Outline platelets.
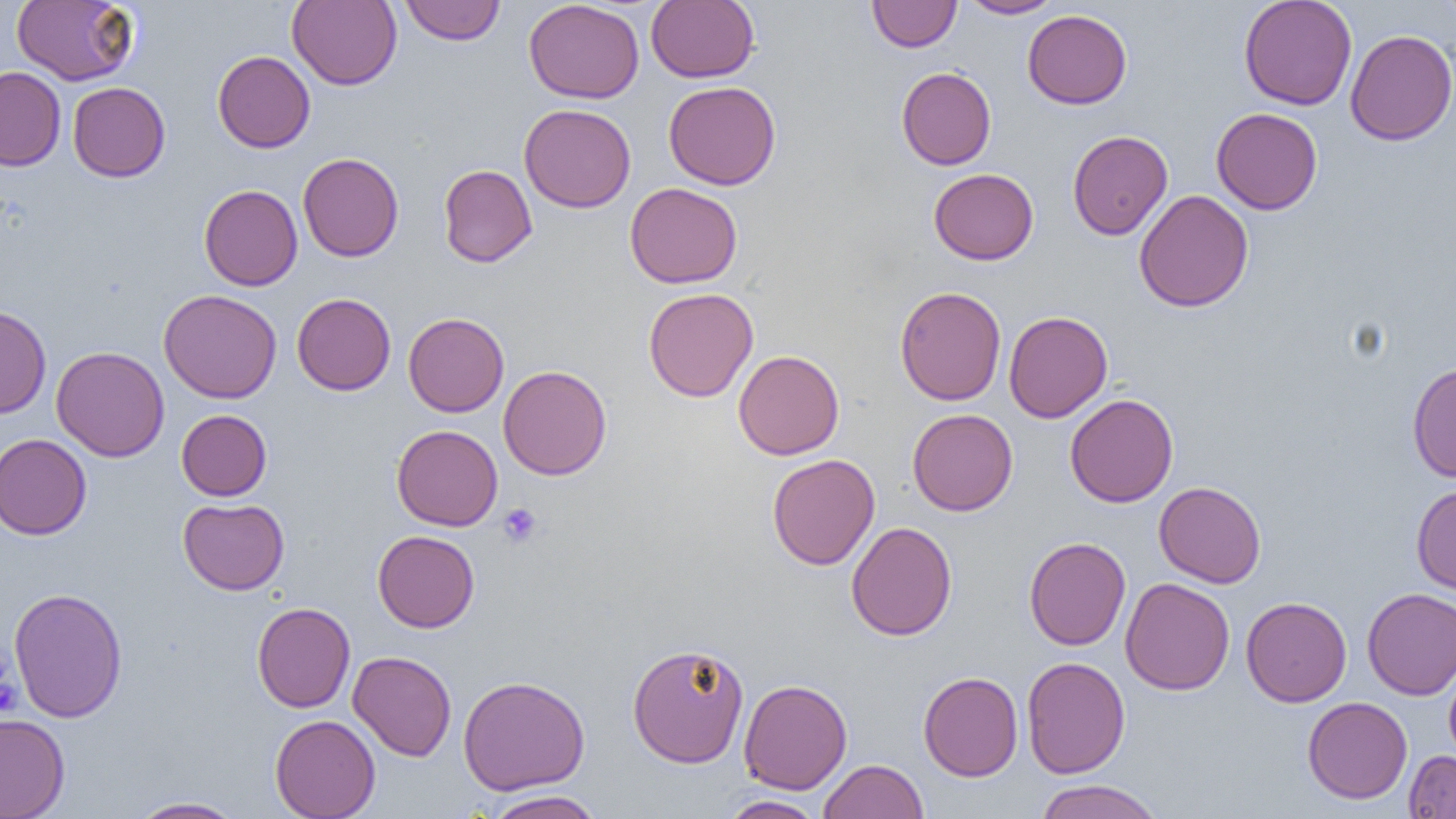

Approximate bounding boxes as named x1/y1/x2/y2 corners in pixels.
Platelets: (x1=498, y1=503, x2=543, y2=548).

Summary:
  - Uninfected red blood cell locations: (x1=11, y1=0, x2=139, y2=86), (x1=288, y1=0, x2=402, y2=90), (x1=400, y1=0, x2=505, y2=45), (x1=523, y1=0, x2=644, y2=103), (x1=867, y1=0, x2=961, y2=52), (x1=959, y1=0, x2=1063, y2=18), (x1=1239, y1=0, x2=1358, y2=110), (x1=1435, y1=0, x2=1456, y2=26), (x1=646, y1=1, x2=760, y2=83), (x1=1022, y1=9, x2=1132, y2=109), (x1=1345, y1=29, x2=1456, y2=146), (x1=212, y1=50, x2=315, y2=152), (x1=0, y1=67, x2=66, y2=171), (x1=896, y1=67, x2=996, y2=170), (x1=663, y1=81, x2=781, y2=190), (x1=68, y1=82, x2=170, y2=182), (x1=519, y1=104, x2=636, y2=213), (x1=1211, y1=108, x2=1323, y2=214), (x1=1067, y1=130, x2=1173, y2=240), (x1=298, y1=152, x2=404, y2=262), (x1=438, y1=164, x2=537, y2=267), (x1=929, y1=168, x2=1038, y2=265), (x1=624, y1=182, x2=743, y2=288), (x1=199, y1=184, x2=302, y2=291), (x1=1134, y1=189, x2=1254, y2=312), (x1=895, y1=286, x2=1006, y2=405), (x1=643, y1=287, x2=758, y2=402), (x1=158, y1=289, x2=282, y2=404), (x1=292, y1=293, x2=396, y2=395), (x1=0, y1=305, x2=52, y2=418), (x1=1004, y1=310, x2=1112, y2=423), (x1=403, y1=312, x2=509, y2=417), (x1=51, y1=345, x2=170, y2=462), (x1=733, y1=350, x2=845, y2=460), (x1=1407, y1=361, x2=1456, y2=483), (x1=498, y1=364, x2=612, y2=480), (x1=1065, y1=393, x2=1179, y2=507), (x1=177, y1=409, x2=272, y2=500), (x1=907, y1=409, x2=1018, y2=515), (x1=392, y1=424, x2=503, y2=531), (x1=0, y1=434, x2=92, y2=540), (x1=767, y1=453, x2=880, y2=570), (x1=1154, y1=481, x2=1266, y2=588), (x1=1411, y1=483, x2=1456, y2=596), (x1=177, y1=498, x2=289, y2=595), (x1=846, y1=521, x2=957, y2=641), (x1=372, y1=530, x2=480, y2=632), (x1=1024, y1=536, x2=1130, y2=650), (x1=1120, y1=577, x2=1235, y2=696), (x1=8, y1=586, x2=128, y2=722), (x1=1362, y1=587, x2=1456, y2=699), (x1=1241, y1=596, x2=1352, y2=707), (x1=252, y1=601, x2=355, y2=712), (x1=627, y1=642, x2=749, y2=767), (x1=347, y1=650, x2=457, y2=761), (x1=1022, y1=656, x2=1130, y2=778), (x1=1444, y1=658, x2=1456, y2=768), (x1=918, y1=671, x2=1024, y2=781), (x1=458, y1=675, x2=590, y2=795), (x1=738, y1=678, x2=852, y2=794), (x1=1302, y1=696, x2=1413, y2=804), (x1=0, y1=714, x2=70, y2=818), (x1=269, y1=714, x2=381, y2=819), (x1=1404, y1=750, x2=1456, y2=818), (x1=817, y1=759, x2=929, y2=819), (x1=1033, y1=779, x2=1165, y2=819), (x1=482, y1=790, x2=605, y2=818), (x1=718, y1=795, x2=826, y2=818), (x1=129, y1=796, x2=246, y2=818)
  - Slide-level diagnosis: no evidence of blood parasites
  - Field of view: single
  - Modality: optical microscopy
  - Magnification: 1000x
  - Image size: 1456×819 pixels
  - Preparation: thin blood smear